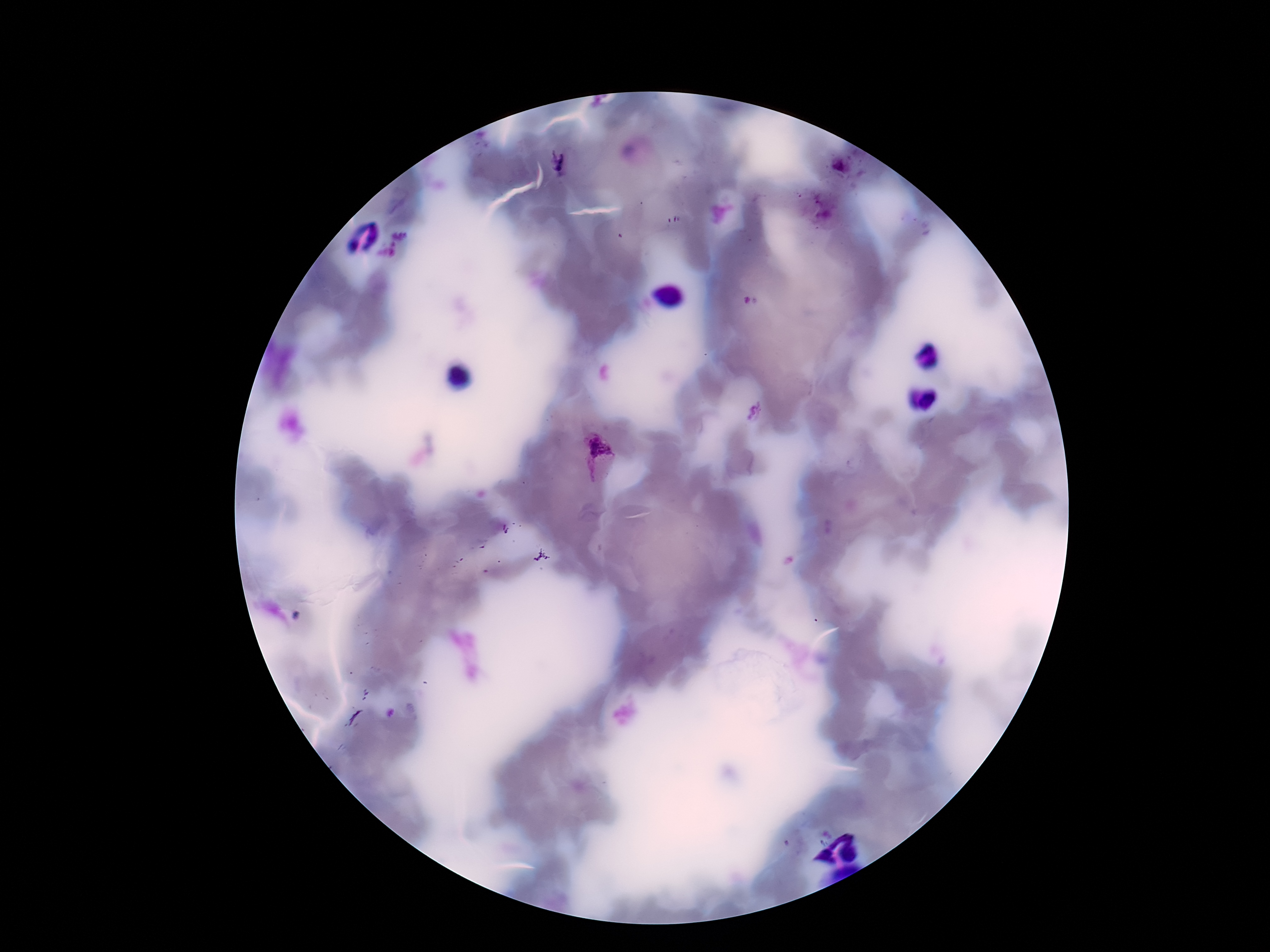

patient malaria status = positive
preparation = thick blood smear
field of view = single
capture = smartphone camera through the microscope eyepiece
Plasmodium parasite locations = approximate centers as {x, y} in pixels: {557, 159}, {841, 166}, {595, 453}
image size = 1270×952 pixels
stain = Giemsa
magnification = 100x